Locate every leukocyte (white blood cell).
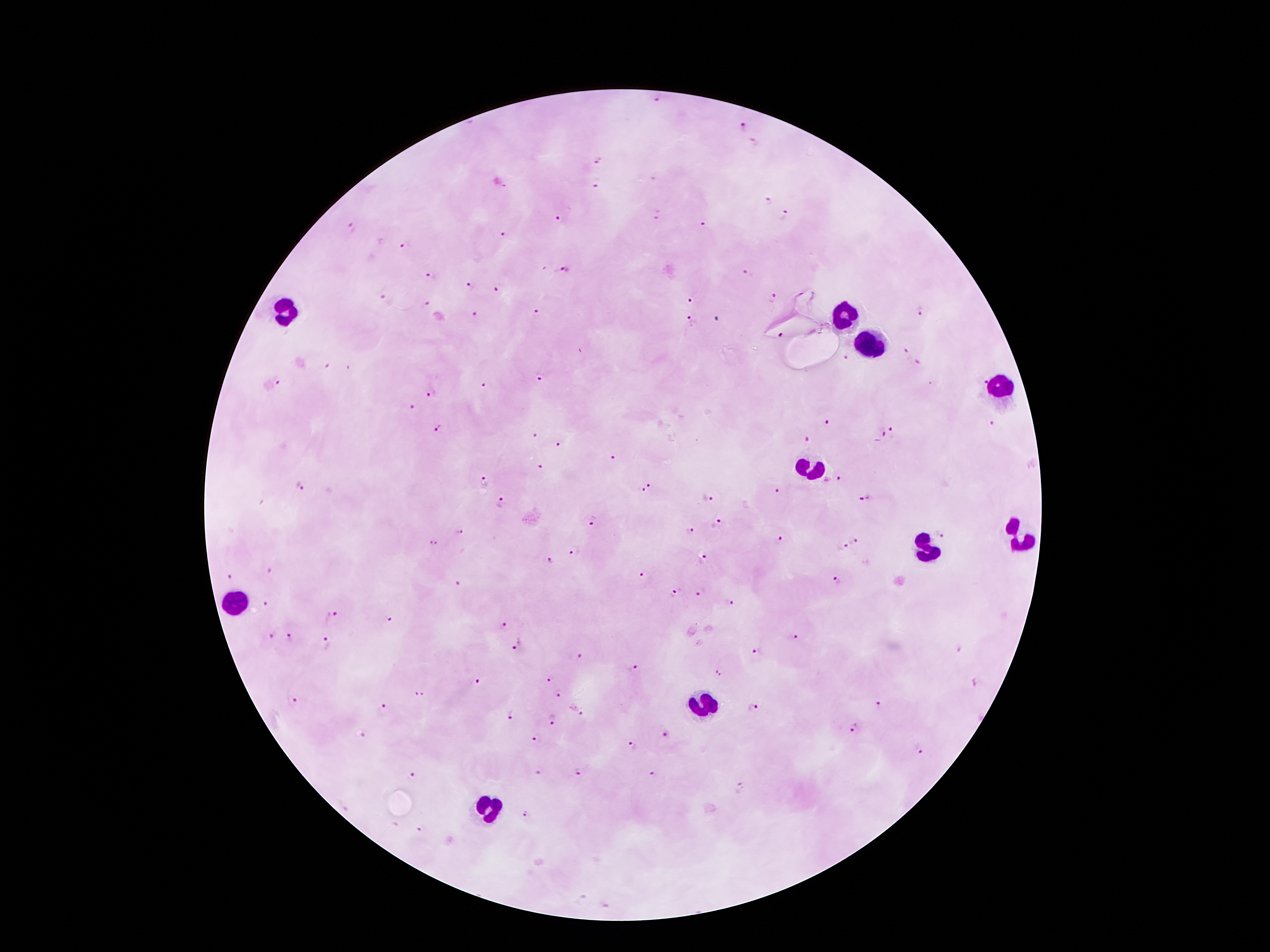

Approximate centers as {x, y} in pixels.
Leukocytes: {286, 308}, {842, 319}, {870, 343}, {999, 386}, {814, 468}, {1021, 537}, {926, 551}, {237, 599}, {704, 705}, {491, 808}.

Summary:
  - Malaria parasite locations: {657, 101}, {743, 124}, {599, 158}, {597, 186}, {767, 202}, {658, 215}, {560, 216}, {786, 217}, {703, 224}, {351, 227}, {504, 235}, {405, 245}, {565, 269}, {748, 273}, {433, 274}, {471, 285}, {499, 286}, {773, 296}, {383, 297}, {691, 300}, {427, 304}, {921, 312}, {476, 313}, {536, 313}, {689, 320}, {781, 334}, {907, 352}, {846, 358}, {918, 363}, {326, 366}, {539, 376}, {277, 381}, {984, 381}, {483, 384}, {433, 393}, {410, 407}, {828, 422}, {993, 424}, {438, 427}, {893, 431}, {884, 434}, {535, 436}, {807, 439}, {558, 446}, {614, 457}, {541, 468}, {840, 478}, {484, 481}, {301, 485}, {651, 486}, {777, 491}, {707, 498}, {866, 499}, {502, 502}, {595, 520}, {716, 523}, {689, 531}, {460, 533}, {941, 533}, {856, 540}, {779, 542}, {433, 544}, {843, 545}, {575, 551}, {704, 557}, {549, 561}, {269, 572}, {644, 575}, {229, 579}, {837, 581}, {454, 582}, {698, 592}, {674, 597}, {732, 603}, {267, 604}, {332, 615}, {389, 619}, {502, 624}, {795, 636}, {270, 637}, {289, 638}, {326, 644}, {518, 647}, {758, 650}, {581, 657}, {633, 668}, {720, 672}, {551, 679}, {477, 681}, {556, 694}, {418, 695}, {294, 700}, {877, 705}, {384, 707}, {753, 708}, {579, 711}, {508, 716}, {555, 718}, {852, 727}, {666, 734}, {363, 735}, {534, 738}, {632, 746}, {921, 748}, {579, 771}, {538, 772}, {654, 773}, {413, 774}, {739, 787}, {525, 815}, {418, 829}
  - Magnification: 100x
  - Stain: Giemsa
  - Preparation: thick blood film
  - Capture: smartphone through the microscope eyepiece
  - Field of view: single
  - Image size: 1270×952 pixels
  - Patient malaria status: infected with Plasmodium falciparum